Point out each leukocyte.
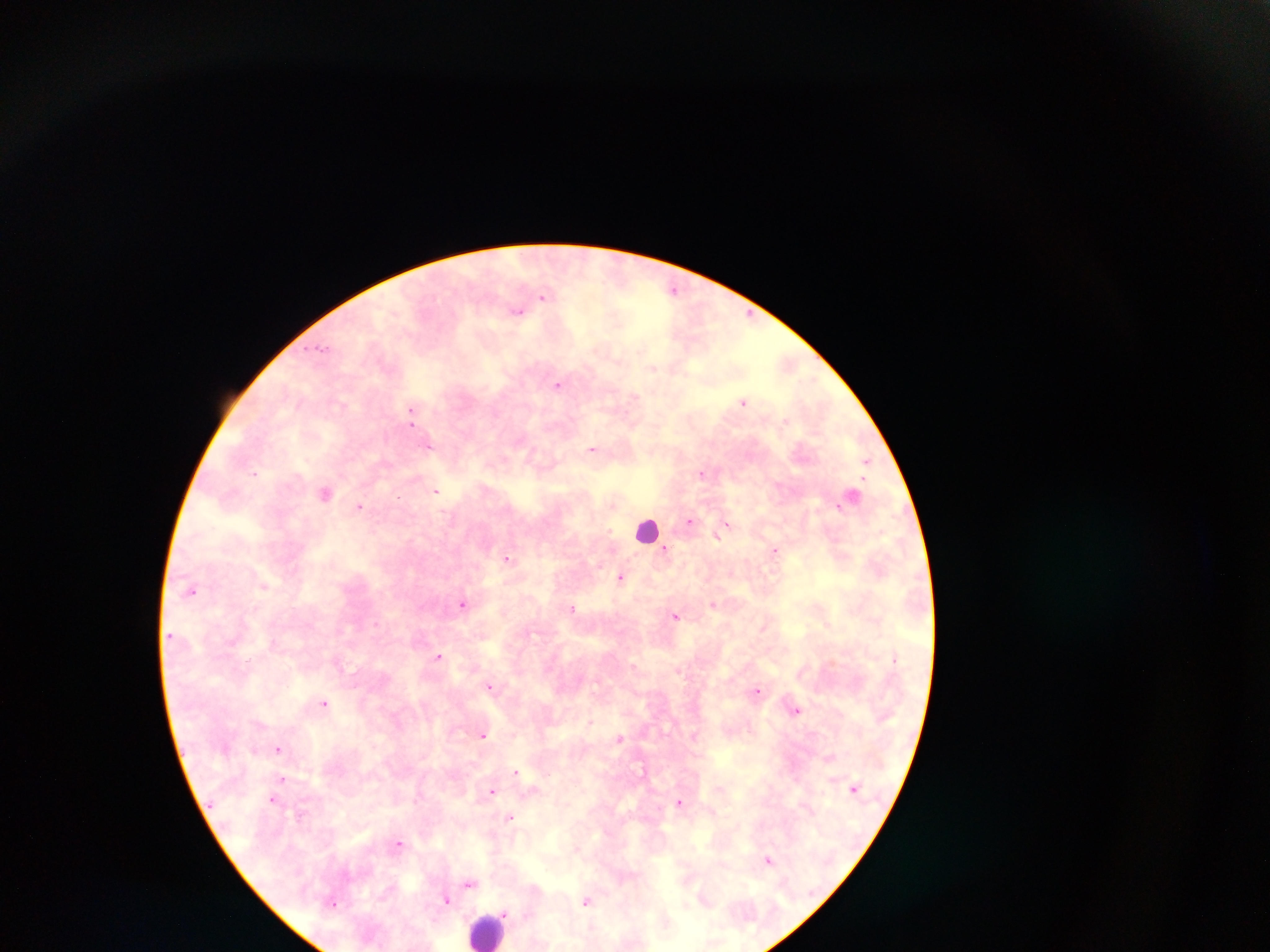
Approximate centers as x y in pixels.
Leukocytes: 646 529; 489 930.

Summary:
  - Plasmodium parasite locations: 674 289; 543 297; 517 312; 749 314; 321 349; 652 368; 557 385; 633 398; 744 402; 411 411; 429 445; 592 449; 866 461; 255 473; 702 473; 436 491; 325 493; 612 505; 359 506; 837 506; 689 522; 726 525; 721 531; 718 536; 665 550; 775 550; 507 558; 621 577; 264 586; 192 591; 713 604; 462 605; 572 608; 675 616; 438 656; 633 666; 490 685; 758 690; 324 703; 796 710; 590 723; 484 735; 619 738; 278 748; 516 771; 282 779; 491 791; 272 799; 680 803; 510 818; 399 843; 768 860; 469 883; 446 900; 586 902; 504 913
  - Image size: 1270×952 pixels
  - Preparation: thick blood film
  - Capture: mobile-phone photograph through a microscope
  - Field of view: single
  - Country: Ghana